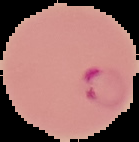

Summary:
  - Preparation: thin blood smear
  - Image type: segmented cell region with the area outside set to black
  - Malaria status: parasitized
  - Image size: 139×142 pixels